Locate every uninfected red blood cell.
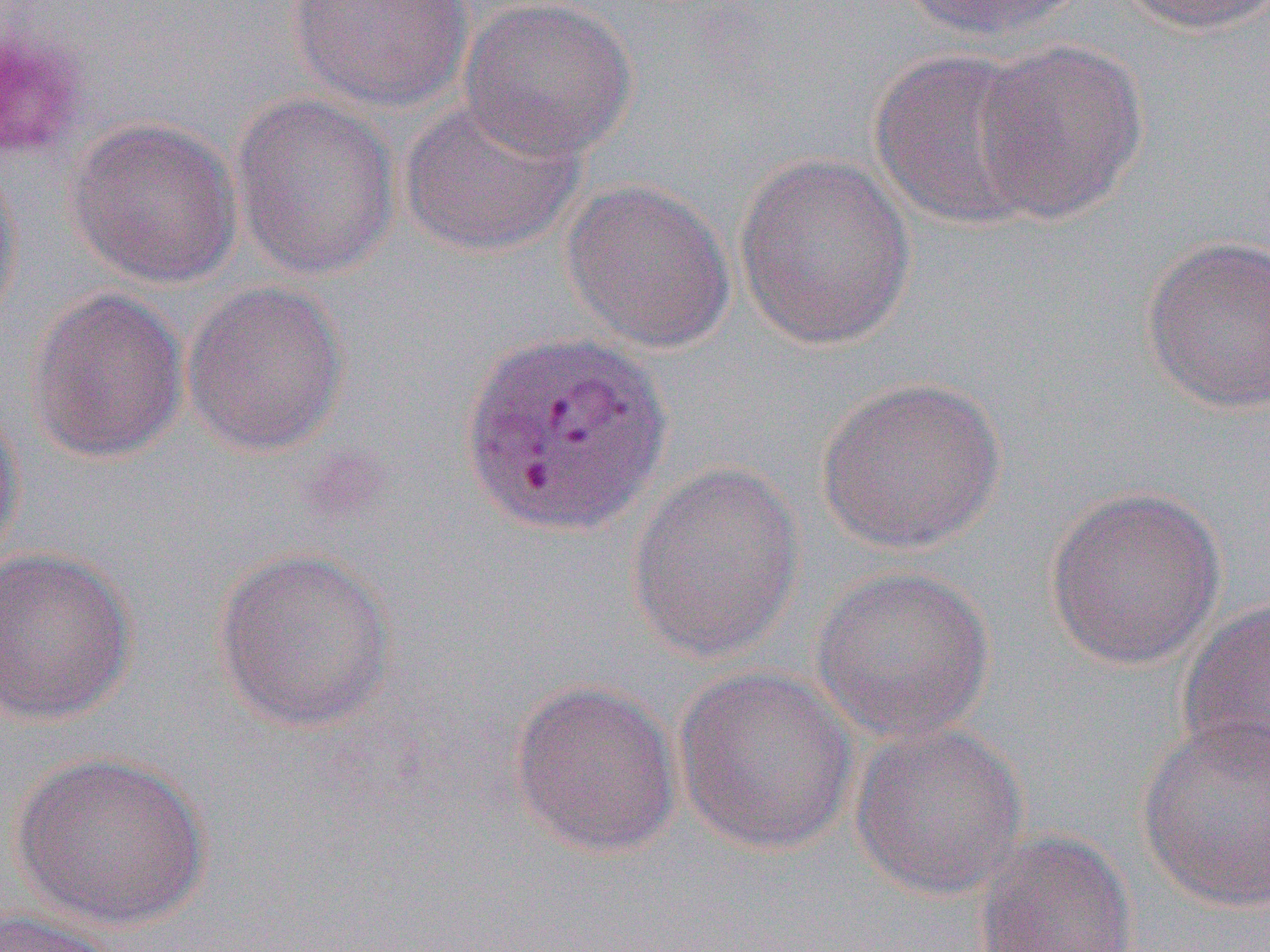

Approximate bounding boxes as (x1, y1, x2, y2) in pixels.
Uninfected red blood cells: (284, 0, 475, 112), (458, 0, 638, 162), (891, 0, 1095, 44), (1114, 0, 1270, 36), (0, 25, 87, 161), (970, 39, 1149, 222), (869, 49, 1053, 231), (230, 91, 402, 280), (398, 95, 588, 259), (66, 118, 243, 288), (733, 152, 916, 351), (0, 155, 24, 334), (561, 178, 736, 355), (1141, 235, 1270, 415), (182, 281, 349, 457), (26, 288, 189, 464), (814, 375, 1007, 555), (0, 397, 26, 573), (625, 461, 806, 664), (1042, 484, 1228, 671), (211, 545, 398, 733), (0, 546, 138, 728), (809, 565, 997, 744), (1175, 597, 1270, 778), (673, 665, 860, 855), (508, 679, 683, 859), (1137, 716, 1269, 913), (849, 722, 1030, 900), (10, 750, 213, 931), (971, 829, 1139, 951), (0, 907, 123, 952).

slide-level diagnosis = Plasmodium vivax
image size = 1270×952 pixels
field of view = single
preparation = thin blood film
modality = light microscopy
magnification = 1000x
platelet locations = approximate bounding boxes as (x1, y1, x2, y2) in pixels: (0, 18, 88, 161)